Comment on the morphology of the erythrocytes.
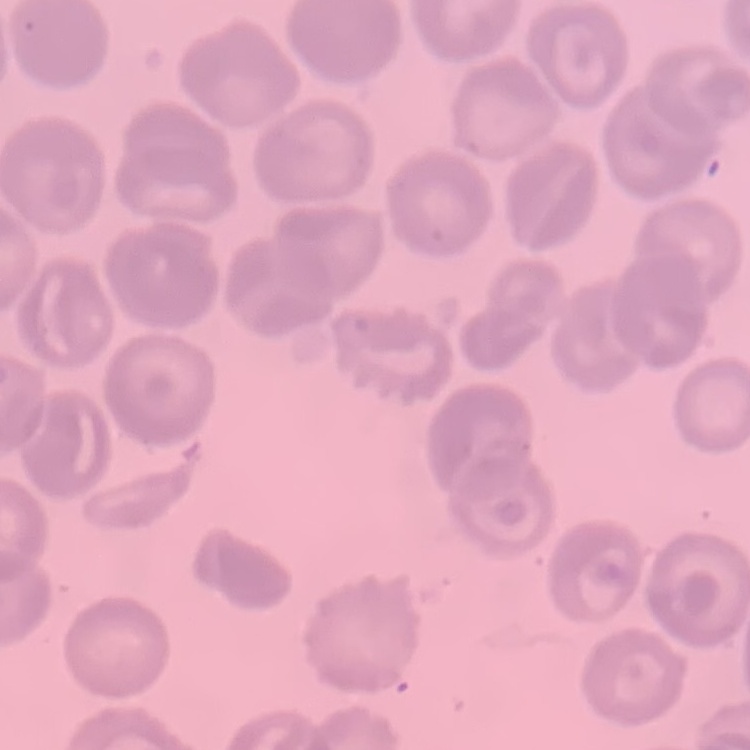
They show no rouleaux formation.

Field's or Giemsa stain. Thin blood film. One tile cut from a larger photomicrograph.